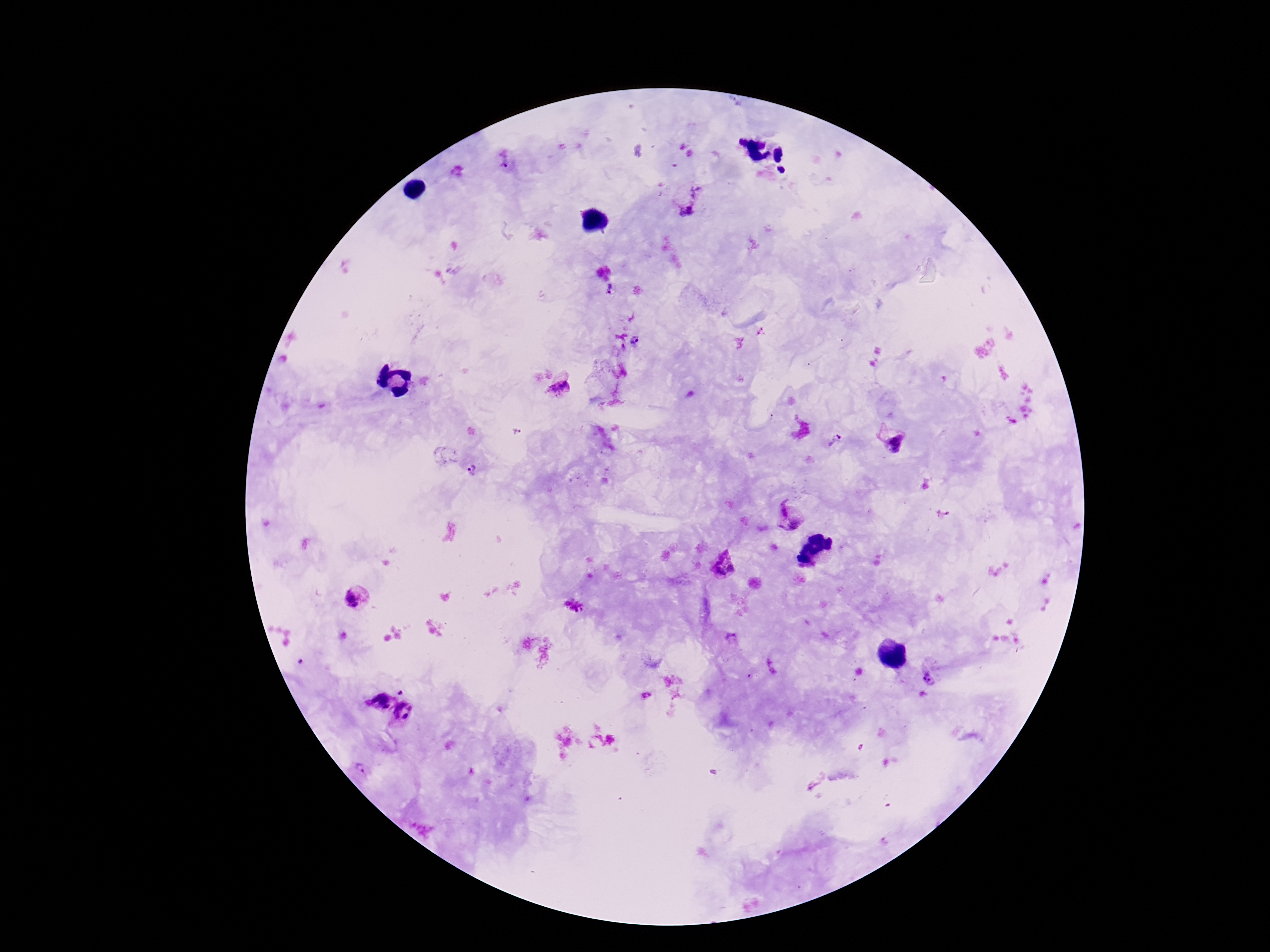
Approximate object centers, in pixels from the top-left corner. Plasmodium parasite locations: (x=505, y=160), (x=697, y=192), (x=686, y=212), (x=610, y=291), (x=638, y=341), (x=559, y=392), (x=835, y=441), (x=896, y=444), (x=473, y=471), (x=788, y=516), (x=724, y=564), (x=354, y=601), (x=574, y=607), (x=773, y=666), (x=929, y=678), (x=402, y=692), (x=646, y=695), (x=378, y=701), (x=407, y=715), (x=362, y=768). 100x magnification. Smartphone photograph taken through the microscope eyepiece. Image is 1270×952 pixels. Giemsa-stained preparation. Patient malaria status: infected. Thick blood film. Single field of view.